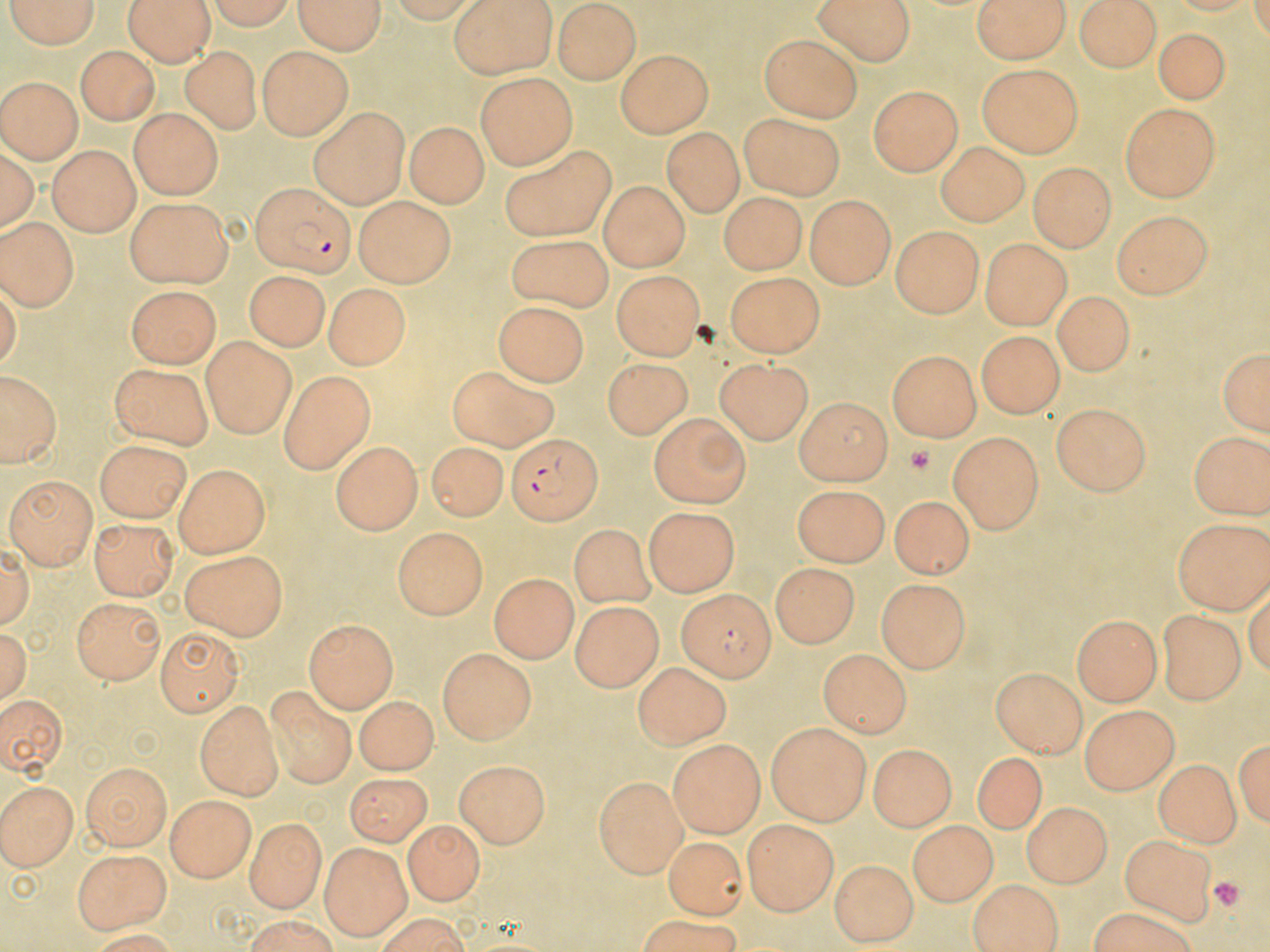

{
  "slide_level_diagnosis": "Plasmodium falciparum",
  "uninfected_red_blood_cell_locations": "approximate bounding boxes as named x1/y1/x2/y2 corners in pixels: (x1=1, y1=0, x2=102, y2=50), (x1=120, y1=0, x2=213, y2=67), (x1=293, y1=0, x2=387, y2=56), (x1=448, y1=0, x2=560, y2=78), (x1=812, y1=0, x2=914, y2=65), (x1=974, y1=0, x2=1069, y2=64), (x1=1075, y1=0, x2=1164, y2=71), (x1=205, y1=1, x2=300, y2=32), (x1=554, y1=3, x2=639, y2=84), (x1=467, y1=8, x2=645, y2=74), (x1=1152, y1=31, x2=1232, y2=106), (x1=760, y1=35, x2=866, y2=122), (x1=73, y1=44, x2=160, y2=125), (x1=259, y1=45, x2=352, y2=139), (x1=183, y1=47, x2=259, y2=132), (x1=616, y1=47, x2=712, y2=137), (x1=975, y1=66, x2=1084, y2=158), (x1=476, y1=72, x2=579, y2=168), (x1=0, y1=75, x2=80, y2=165), (x1=866, y1=85, x2=961, y2=175), (x1=1120, y1=101, x2=1224, y2=201), (x1=309, y1=107, x2=408, y2=207), (x1=130, y1=110, x2=221, y2=197), (x1=738, y1=111, x2=847, y2=197), (x1=406, y1=121, x2=487, y2=206), (x1=661, y1=131, x2=745, y2=215), (x1=934, y1=141, x2=1026, y2=226), (x1=47, y1=145, x2=141, y2=234), (x1=501, y1=147, x2=618, y2=242), (x1=1026, y1=162, x2=1119, y2=249), (x1=601, y1=182, x2=688, y2=273), (x1=715, y1=191, x2=807, y2=273), (x1=803, y1=194, x2=893, y2=287), (x1=124, y1=195, x2=231, y2=289), (x1=353, y1=197, x2=456, y2=282), (x1=1112, y1=208, x2=1213, y2=302), (x1=0, y1=215, x2=78, y2=313), (x1=889, y1=229, x2=984, y2=316), (x1=504, y1=235, x2=613, y2=311), (x1=979, y1=242, x2=1070, y2=327), (x1=244, y1=268, x2=328, y2=348), (x1=724, y1=271, x2=822, y2=356), (x1=611, y1=273, x2=704, y2=358), (x1=326, y1=287, x2=404, y2=367), (x1=129, y1=289, x2=217, y2=367), (x1=1053, y1=289, x2=1129, y2=376), (x1=495, y1=301, x2=591, y2=384), (x1=981, y1=328, x2=1070, y2=417), (x1=202, y1=337, x2=295, y2=437), (x1=1216, y1=345, x2=1269, y2=438), (x1=887, y1=353, x2=979, y2=443), (x1=717, y1=356, x2=818, y2=443), (x1=601, y1=358, x2=695, y2=436), (x1=107, y1=364, x2=217, y2=452), (x1=447, y1=364, x2=561, y2=447), (x1=280, y1=371, x2=369, y2=473), (x1=3, y1=374, x2=57, y2=466), (x1=793, y1=397, x2=892, y2=484), (x1=1051, y1=405, x2=1152, y2=494), (x1=644, y1=415, x2=747, y2=503), (x1=1188, y1=426, x2=1269, y2=519), (x1=950, y1=431, x2=1043, y2=536), (x1=332, y1=440, x2=420, y2=533), (x1=95, y1=441, x2=193, y2=521), (x1=423, y1=445, x2=505, y2=522), (x1=172, y1=461, x2=266, y2=554), (x1=5, y1=478, x2=95, y2=567), (x1=792, y1=487, x2=887, y2=563), (x1=889, y1=491, x2=970, y2=576), (x1=642, y1=510, x2=738, y2=594), (x1=1174, y1=516, x2=1269, y2=612), (x1=88, y1=518, x2=174, y2=601), (x1=569, y1=523, x2=651, y2=611), (x1=391, y1=529, x2=486, y2=619), (x1=180, y1=547, x2=286, y2=639), (x1=769, y1=567, x2=856, y2=649), (x1=487, y1=575, x2=578, y2=660), (x1=880, y1=578, x2=973, y2=671), (x1=67, y1=598, x2=160, y2=683), (x1=573, y1=603, x2=658, y2=692), (x1=1156, y1=609, x2=1240, y2=707), (x1=1070, y1=615, x2=1161, y2=707), (x1=304, y1=618, x2=396, y2=712), (x1=159, y1=628, x2=238, y2=717), (x1=820, y1=647, x2=907, y2=739), (x1=438, y1=648, x2=534, y2=745), (x1=636, y1=664, x2=727, y2=749), (x1=990, y1=669, x2=1088, y2=753), (x1=265, y1=686, x2=355, y2=790), (x1=0, y1=689, x2=63, y2=780), (x1=356, y1=697, x2=440, y2=778), (x1=197, y1=702, x2=281, y2=798), (x1=1079, y1=706, x2=1179, y2=791), (x1=764, y1=722, x2=870, y2=822), (x1=1235, y1=728, x2=1268, y2=835), (x1=668, y1=741, x2=767, y2=837), (x1=870, y1=743, x2=956, y2=829), (x1=972, y1=749, x2=1045, y2=835), (x1=1156, y1=756, x2=1238, y2=845), (x1=456, y1=760, x2=546, y2=849), (x1=83, y1=764, x2=170, y2=849), (x1=343, y1=773, x2=434, y2=844), (x1=594, y1=778, x2=684, y2=878), (x1=0, y1=779, x2=80, y2=869), (x1=165, y1=798, x2=254, y2=879), (x1=1022, y1=802, x2=1113, y2=883), (x1=244, y1=819, x2=325, y2=910), (x1=743, y1=820, x2=838, y2=914), (x1=403, y1=821, x2=484, y2=903), (x1=907, y1=821, x2=993, y2=903), (x1=1120, y1=832, x2=1216, y2=921), (x1=662, y1=836, x2=742, y2=920), (x1=320, y1=842, x2=409, y2=939), (x1=71, y1=845, x2=169, y2=933), (x1=831, y1=859, x2=914, y2=945), (x1=967, y1=880, x2=1065, y2=952), (x1=1082, y1=911, x2=1205, y2=952), (x1=623, y1=918, x2=759, y2=952)",
  "preparation": "thin blood film",
  "stain": "May-Grünwald-Giemsa",
  "platelet_locations": "approximate bounding boxes as named x1/y1/x2/y2 corners in pixels: (x1=907, y1=447, x2=935, y2=474), (x1=1210, y1=877, x2=1246, y2=908)",
  "plasmodium_falciparum_infected_red_blood_cell_locations": "approximate bounding boxes as named x1/y1/x2/y2 corners in pixels: (x1=249, y1=184, x2=355, y2=278), (x1=509, y1=434, x2=601, y2=521), (x1=676, y1=591, x2=778, y2=676)",
  "modality": "optical microscopy",
  "image_size": "1270×952 pixels",
  "field_of_view": "single",
  "magnification": "1000x"
}